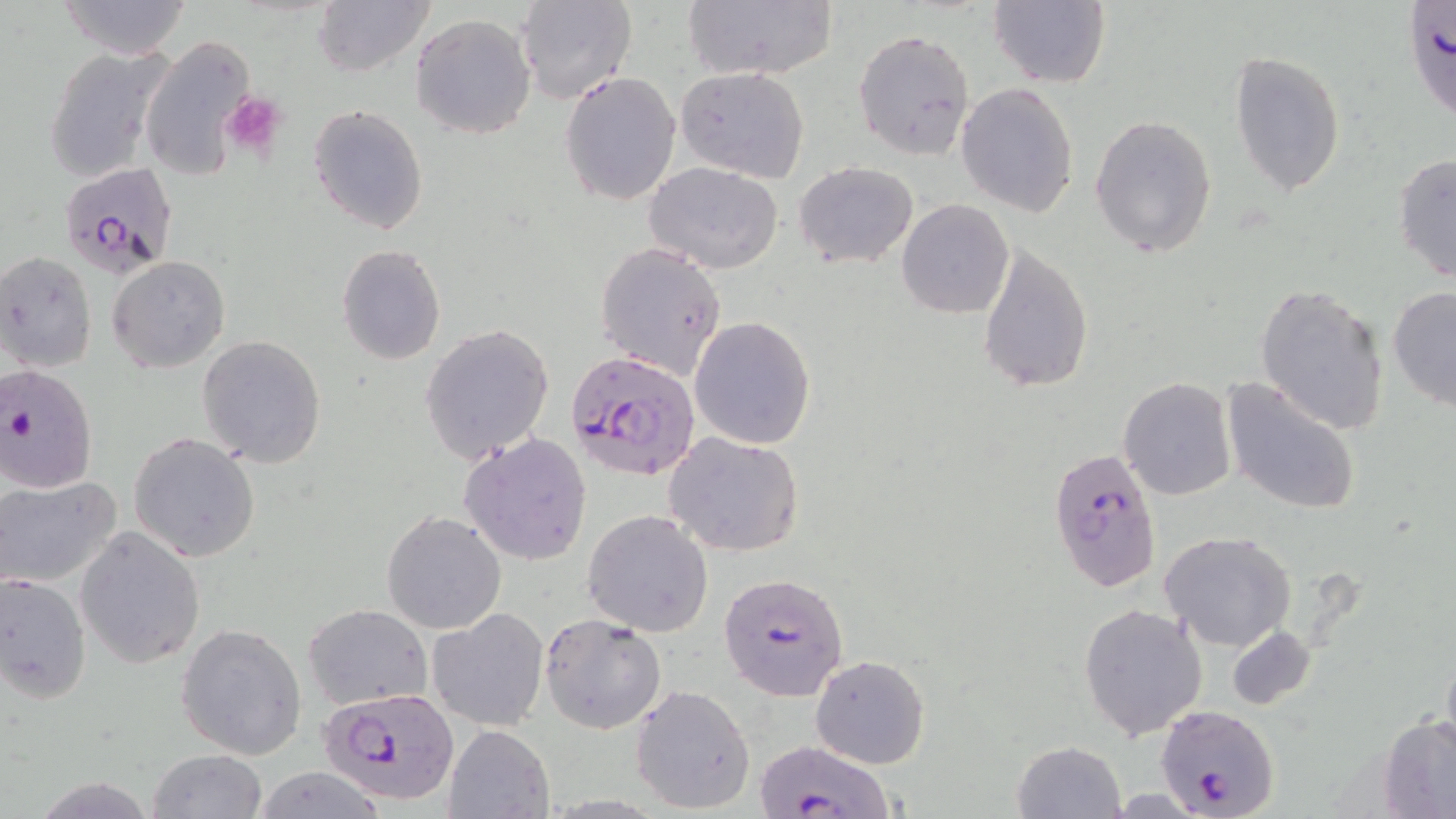
Approximate bounding boxes as (x1,y1)-(x2,y2) corner pairs in pixels. Platelet locations: (221,91)-(286,164). Uninfected red blood cell locations: (57,0)-(192,59), (682,0)-(836,82), (989,0)-(1110,88), (313,1)-(434,78), (514,1)-(637,105), (410,13)-(536,140), (853,28)-(976,163), (140,36)-(254,181), (43,43)-(174,183), (1229,50)-(1346,196), (675,66)-(811,183), (561,71)-(681,205), (956,82)-(1080,218), (308,104)-(429,234), (1090,114)-(1217,259), (1392,154)-(1456,284), (794,161)-(919,270), (644,163)-(784,274), (897,200)-(1014,318), (978,240)-(1094,394), (594,242)-(727,378), (336,245)-(447,366), (0,251)-(99,373), (106,255)-(231,374), (1255,282)-(1389,437), (1387,284)-(1456,413), (689,317)-(816,450), (420,325)-(554,467), (198,335)-(327,467), (1220,376)-(1362,514), (1119,378)-(1235,501), (663,430)-(805,557), (460,432)-(592,565), (129,433)-(261,562), (0,473)-(125,590), (582,509)-(714,636), (381,511)-(506,633), (74,526)-(206,670), (1159,530)-(1297,651), (0,574)-(91,702), (1078,602)-(1207,741), (304,603)-(432,711), (428,608)-(550,731), (540,614)-(668,735), (177,622)-(308,759), (1225,625)-(1314,710), (1441,645)-(1456,755), (810,654)-(930,769), (630,683)-(756,814), (1381,714)-(1456,816), (443,724)-(554,819), (1012,739)-(1126,818), (147,749)-(266,819), (247,768)-(390,818). Plasmodium falciparum-infected red blood cell locations: (1406,5)-(1455,126), (57,161)-(177,278), (567,350)-(699,484), (0,364)-(100,492), (1047,446)-(1160,593), (719,572)-(850,700), (319,688)-(461,807), (1157,702)-(1281,818), (753,741)-(891,817). Slide-level diagnosis: Plasmodium falciparum. 1000x magnification. One field of a larger specimen. Thin blood smear. May-Grünwald-Giemsa-stained preparation. Image is 1456×819 pixels. Light microscopy.